Describe the morphology of the red blood cells.
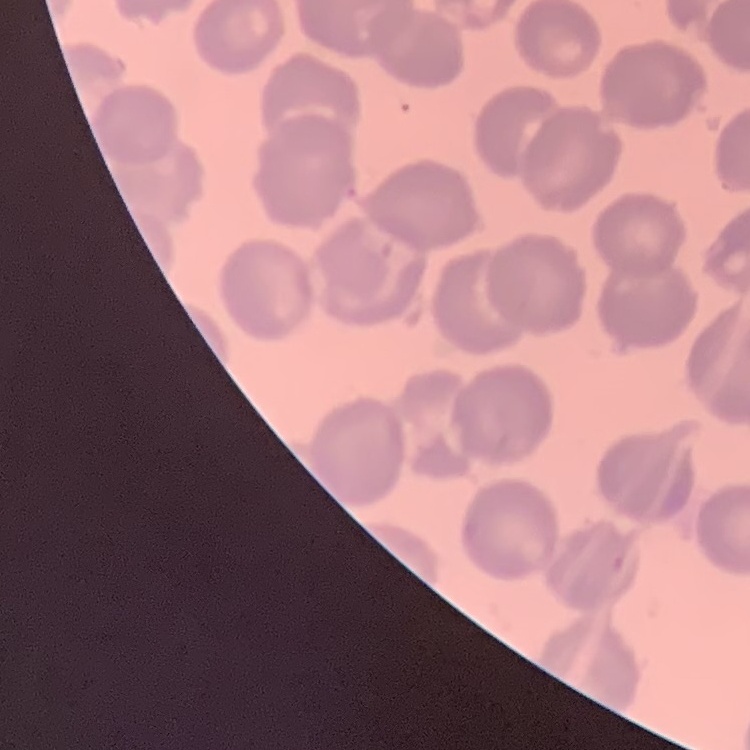
They show no rouleaux formation.

Field's or Giemsa stain. Square crop of a larger photomicrograph. Thin blood film.